Assess this cell for malaria.
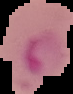
Parasitized.

Summary:
  - Preparation: thin blood film
  - Image type: segmented cell region on a black background
  - Image size: 73×94 pixels